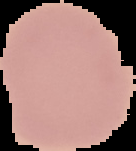

{
  "image_type": "cell region segmented out of the field of view; surrounding area masked to black",
  "preparation": "thin blood film",
  "result": "no malaria parasites seen",
  "image_size": "136×151 pixels"
}